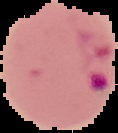

preparation: thin blood film
image_size: 118×133 pixels
malaria_status: parasitized
image_type: cell region segmented out of the field of view; surrounding area masked to black